Locate every Plasmodium falciparum-infected red blood cell.
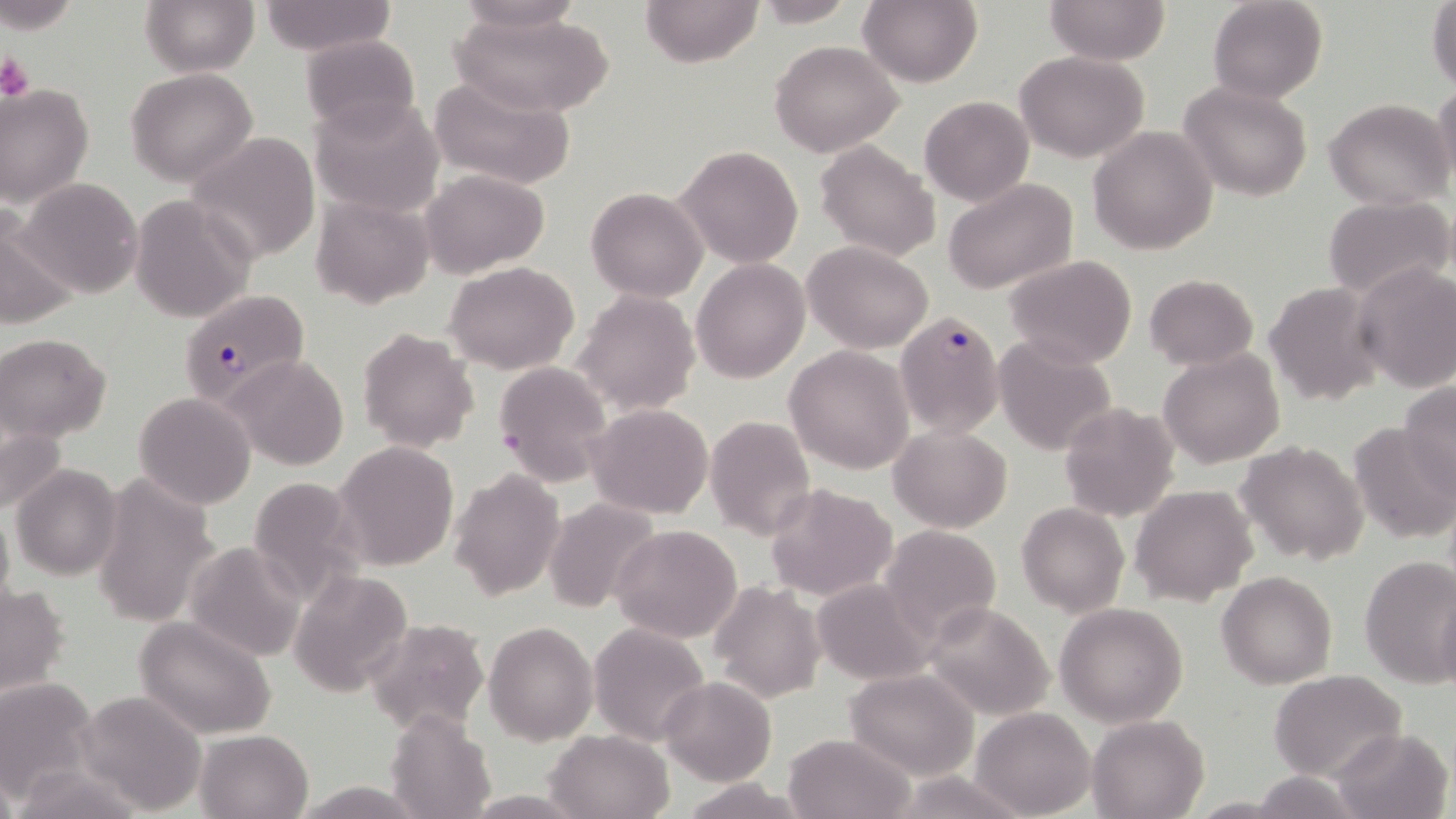

Approximate bounding boxes as [x1, y1, x2, y2] in pixels.
Plasmodium falciparum-infected red blood cells: [178, 289, 309, 407], [896, 311, 1006, 436].

{
  "slide_level_diagnosis": "Plasmodium falciparum",
  "modality": "optical microscopy",
  "stain": "May-Grünwald-Giemsa",
  "magnification": "1000x",
  "field_of_view": "one of a larger specimen",
  "uninfected_red_blood_cell_locations": "approximate bounding boxes as [x1, y1, x2, y2] in pixels: [141, 0, 258, 76], [455, 0, 586, 36], [639, 0, 764, 68], [751, 0, 863, 26], [858, 0, 983, 88], [1044, 0, 1169, 66], [1207, 0, 1329, 103], [1427, 0, 1456, 93], [255, 2, 395, 55], [450, 11, 616, 118], [301, 35, 423, 137], [769, 40, 903, 157], [1015, 51, 1150, 162], [126, 68, 258, 186], [429, 74, 577, 191], [1177, 81, 1315, 203], [1433, 82, 1456, 192], [1, 84, 94, 208], [919, 95, 1033, 207], [309, 96, 445, 218], [1325, 97, 1454, 209], [1088, 126, 1219, 256], [184, 133, 321, 264], [816, 141, 941, 262], [674, 146, 803, 267], [421, 169, 548, 278], [14, 177, 143, 298], [943, 178, 1079, 295], [587, 186, 708, 301], [310, 193, 436, 310], [129, 196, 256, 323], [1324, 196, 1456, 301], [0, 212, 79, 332], [803, 241, 933, 352], [1005, 255, 1137, 369], [691, 258, 809, 384], [443, 260, 579, 374], [1354, 264, 1456, 393], [1145, 273, 1257, 370], [1264, 282, 1384, 405], [574, 289, 699, 414], [358, 328, 479, 453], [0, 332, 113, 443], [994, 337, 1116, 457], [784, 344, 915, 474], [1159, 349, 1285, 468], [223, 353, 351, 472], [493, 359, 614, 488], [1399, 379, 1456, 498], [134, 392, 256, 508], [1060, 401, 1180, 521], [586, 403, 714, 518], [1, 410, 71, 520], [704, 415, 815, 540], [1347, 420, 1453, 544], [890, 425, 1013, 533], [1236, 440, 1369, 567], [331, 441, 460, 570], [11, 464, 124, 581], [448, 468, 565, 601], [89, 471, 221, 627], [242, 475, 370, 607], [764, 483, 897, 602], [1129, 484, 1259, 604], [541, 496, 663, 613], [0, 501, 14, 618], [1016, 501, 1130, 617], [611, 524, 743, 644], [880, 524, 1002, 643], [184, 542, 306, 662], [1359, 555, 1456, 687], [289, 571, 414, 697], [1218, 571, 1338, 689], [812, 578, 935, 685], [1, 581, 72, 699], [709, 581, 826, 703], [1435, 588, 1456, 693], [923, 599, 1057, 721], [1053, 602, 1189, 727], [135, 616, 276, 739], [362, 618, 489, 733], [484, 621, 597, 746], [589, 623, 710, 747], [844, 666, 979, 780], [1269, 670, 1408, 781], [659, 677, 776, 785], [0, 678, 98, 801], [74, 691, 206, 815], [970, 706, 1094, 818], [387, 708, 497, 819], [1089, 715, 1208, 819], [1332, 727, 1453, 818], [545, 729, 674, 819], [194, 730, 312, 818], [782, 733, 915, 819], [0, 765, 22, 819], [11, 765, 149, 817], [890, 770, 1027, 819], [1248, 771, 1361, 817], [678, 778, 812, 817], [293, 780, 423, 817], [458, 790, 593, 817], [1184, 797, 1299, 817]",
  "image_size": "1456×819 pixels",
  "platelet_locations": "approximate bounding boxes as [x1, y1, x2, y2] in pixels: [0, 51, 35, 100]",
  "preparation": "thin blood film"
}